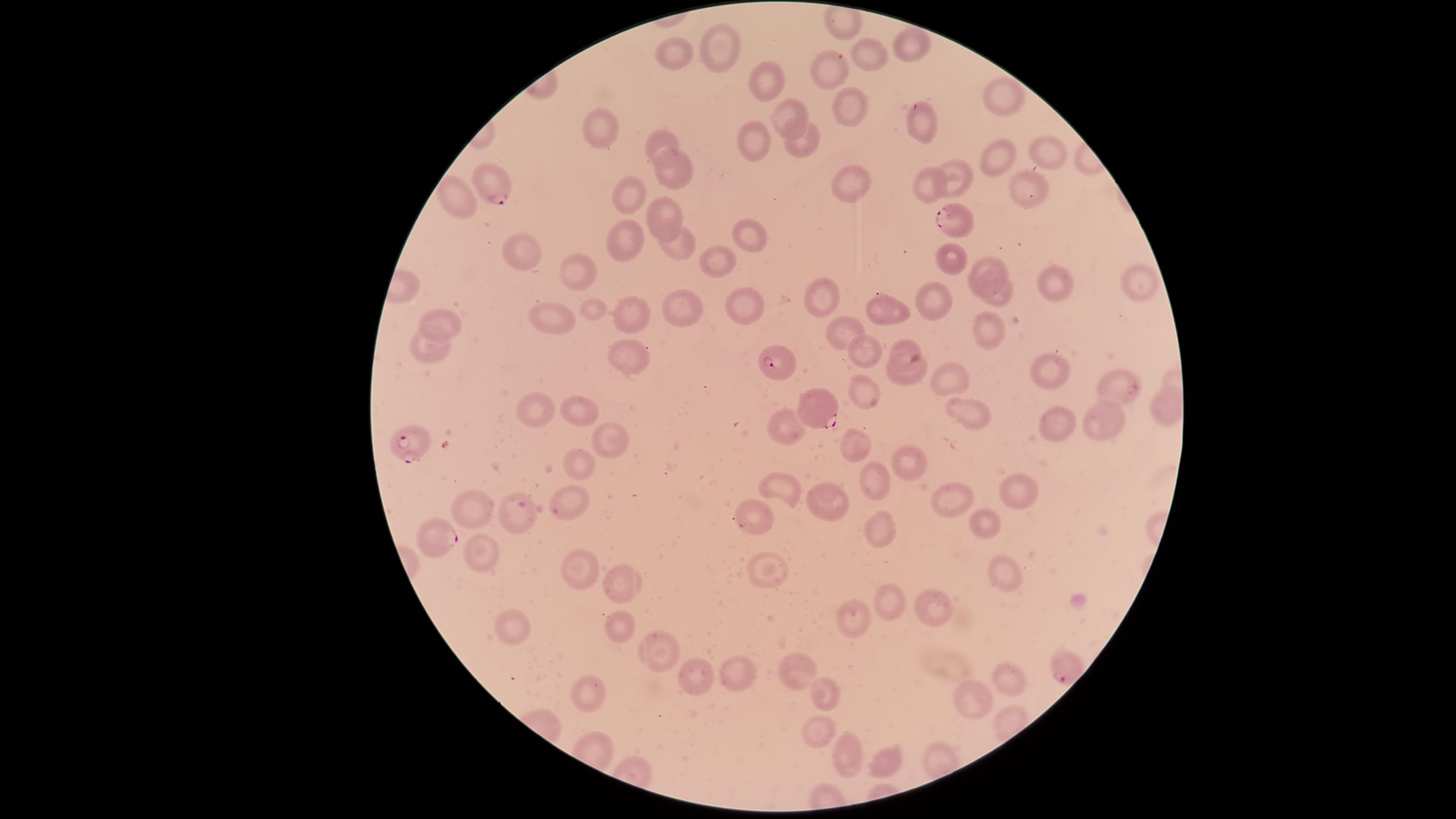
Approximate marker points, in pixels from the top-left corner.
Summary:
  - Uninfected red blood cells: (x=723, y=44), (x=910, y=44), (x=673, y=51), (x=871, y=58), (x=834, y=67), (x=768, y=74), (x=1007, y=97), (x=849, y=103), (x=787, y=120), (x=928, y=123), (x=607, y=127), (x=663, y=140), (x=805, y=143), (x=758, y=145), (x=1050, y=154), (x=1002, y=163), (x=674, y=172), (x=961, y=176), (x=849, y=183), (x=928, y=188), (x=1028, y=188), (x=631, y=196), (x=466, y=203), (x=670, y=214), (x=752, y=236), (x=621, y=238), (x=677, y=248), (x=523, y=250), (x=717, y=253), (x=951, y=254), (x=991, y=267), (x=583, y=268), (x=1145, y=284), (x=1059, y=289), (x=827, y=293), (x=930, y=297), (x=1002, y=300), (x=596, y=307), (x=681, y=310), (x=740, y=310), (x=892, y=313), (x=633, y=314), (x=446, y=322), (x=558, y=322), (x=993, y=332), (x=847, y=339), (x=901, y=349), (x=432, y=357), (x=629, y=359), (x=867, y=360), (x=1044, y=365), (x=951, y=375), (x=909, y=380), (x=1117, y=386), (x=869, y=394), (x=1163, y=405), (x=585, y=412), (x=1096, y=414), (x=969, y=415), (x=533, y=417), (x=792, y=420), (x=1056, y=422), (x=619, y=439), (x=853, y=447), (x=911, y=461), (x=582, y=465), (x=779, y=485), (x=871, y=487), (x=1012, y=490), (x=569, y=492), (x=825, y=498), (x=953, y=498), (x=478, y=507), (x=518, y=518), (x=753, y=518), (x=980, y=524), (x=884, y=530), (x=478, y=547), (x=577, y=565), (x=764, y=572), (x=1003, y=576), (x=617, y=581), (x=886, y=601), (x=934, y=609), (x=851, y=621), (x=518, y=628), (x=622, y=629), (x=648, y=650), (x=738, y=671), (x=796, y=672), (x=1011, y=674), (x=705, y=675), (x=593, y=688), (x=830, y=696), (x=977, y=699), (x=811, y=733), (x=847, y=753), (x=889, y=761)
  - Parasitized red blood cells: (x=488, y=184), (x=954, y=222), (x=776, y=362), (x=818, y=405), (x=412, y=442), (x=438, y=535)
  - Visible region: circular
  - Preparation: thin blood film
  - Stain: Giemsa
  - Capture: smartphone photograph through the microscope eyepiece
  - Image size: 1456×819 pixels
  - Presence: malaria parasites identified
  - Species: Plasmodium falciparum
  - Field of view: single